State which cell type is depicted.
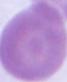
An erythrocyte.

Captured at 1000x magnification. Micrograph.